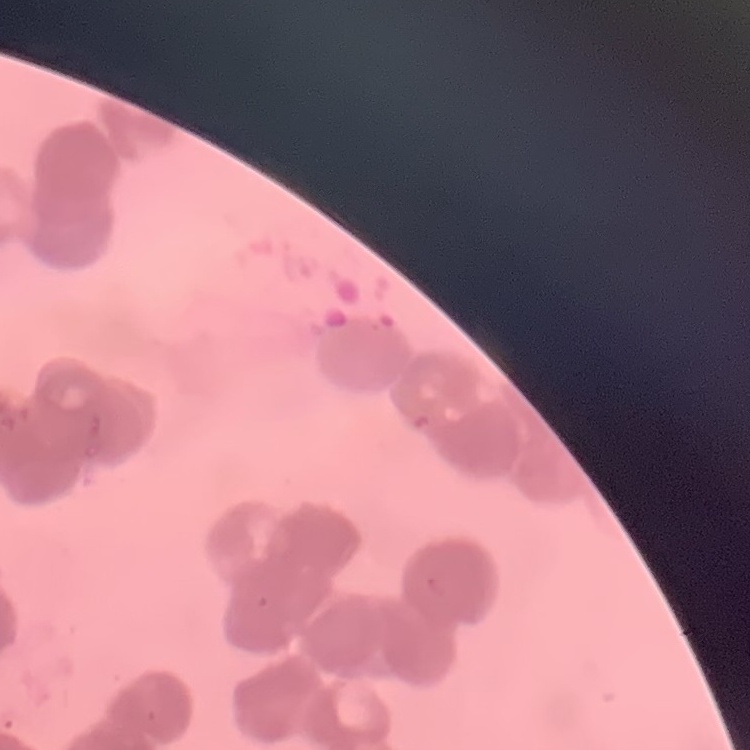
The red blood cells exhibit rouleaux formation. One tile cut from a larger photomicrograph. Stained with either Field's or Giemsa. Thin blood smear.